Describe the morphology of the red blood cells.
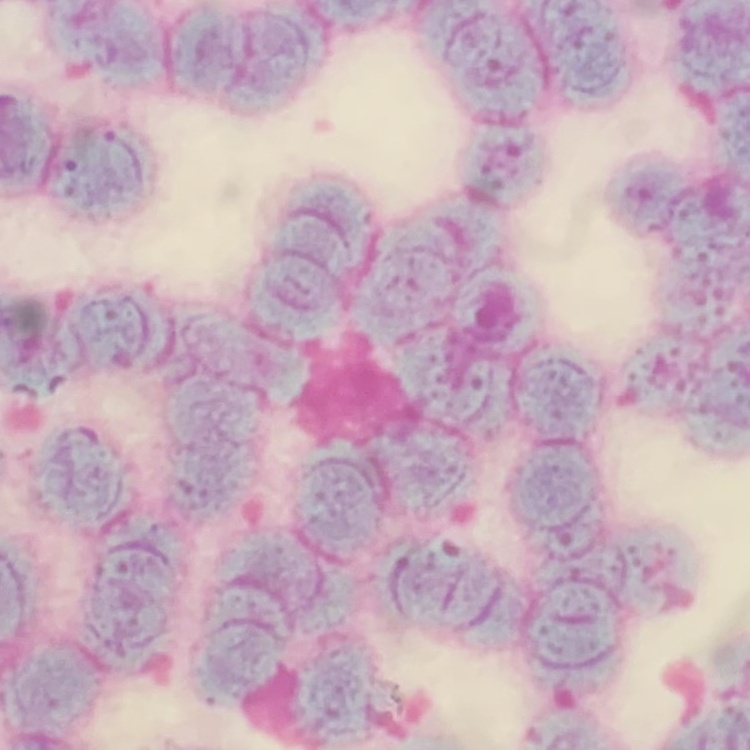
Rouleaux formation.

Summary:
  - Stain: Field's or Giemsa
  - Preparation: thin blood smear
  - Image type: square crop of a larger photomicrograph